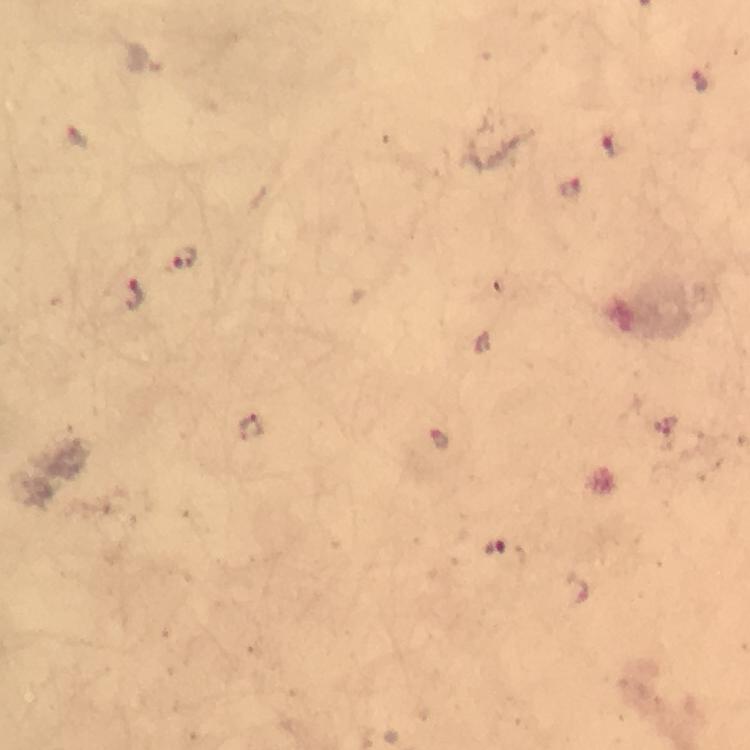
Approximate centers as (x, y) in pixels. Malaria parasite locations: (699, 82), (77, 137), (611, 145), (574, 189), (186, 258), (135, 296), (250, 429), (439, 442), (496, 548). At 100x magnification. Immersion oil was used. Photographed through the microscope with a smartphone camera. Image is 750×750 pixels. Giemsa-stained preparation. Thick blood smear. A crop from one field of view. From a diagnostic examination for malaria.